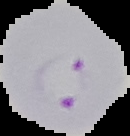

{
  "image_type": "segmented cell region on a black background",
  "preparation": "thin blood film",
  "image_size": "130×136 pixels",
  "result": "malaria parasites identified"
}